Locate every blood parasite and identify its species.
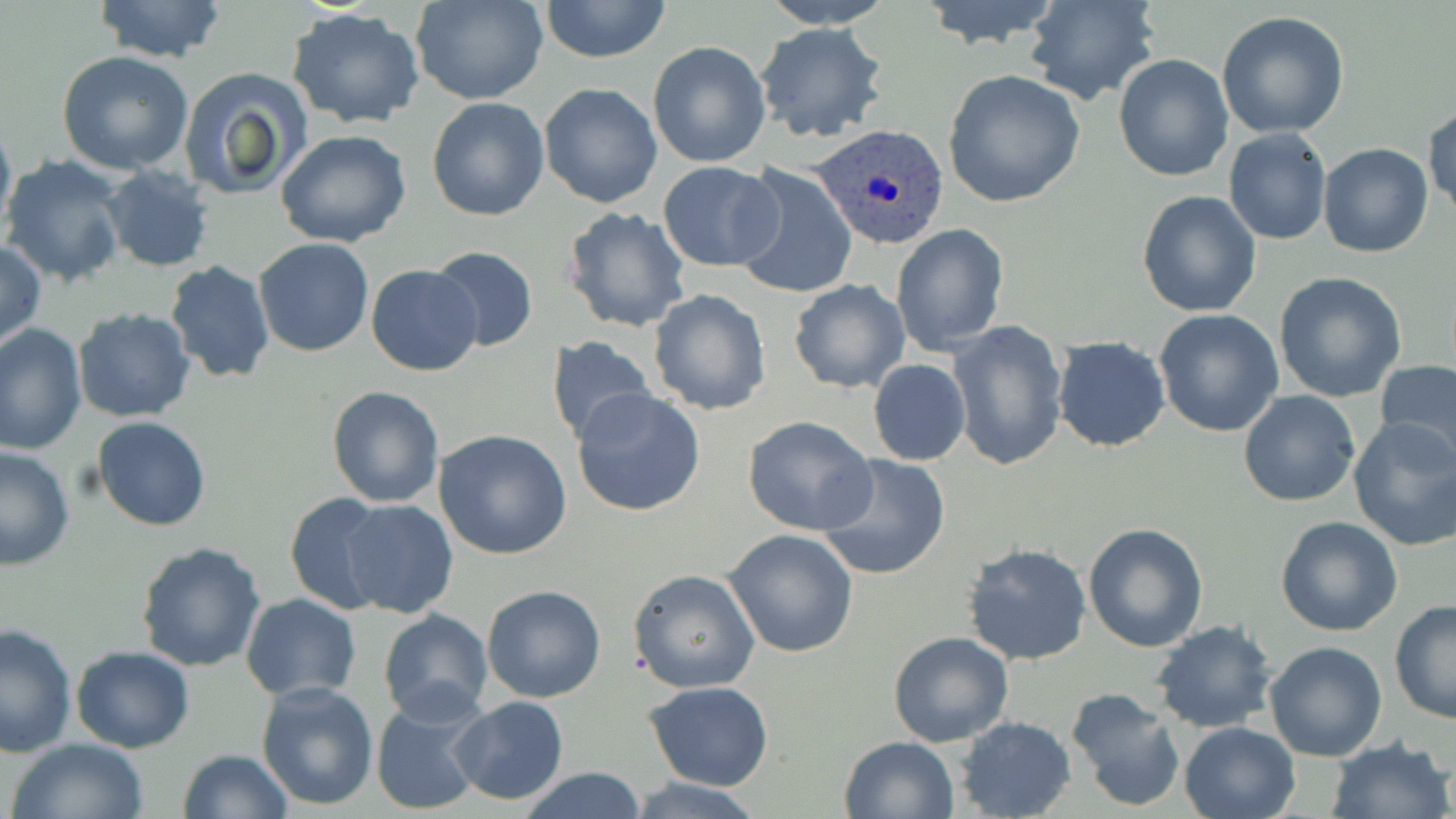

Approximate bounding boxes as (x1,y1)-(x2,y2) corner pairs in pixels.
Plasmodium ovale-infected red blood cells: (812,125)-(952,250).
No Plasmodium falciparum, Plasmodium malariae, Plasmodium vivax, Babesia divergens, or Trypanosoma brucei observed.

{
  "slide_level_diagnosis": "Plasmodium ovale",
  "field_of_view": "single",
  "modality": "optical microscopy",
  "magnification": "1000x",
  "stain": "May-Grünwald-Giemsa",
  "preparation": "thin blood smear",
  "uninfected_red_blood_cell_locations": "approximate bounding boxes as (x1,y1)-(x2,y2) corner pairs in pixels: (93,0)-(229,63), (413,0)-(550,105), (539,0)-(671,63), (758,0)-(899,28), (917,0)-(1066,52), (1023,0)-(1162,105), (285,8)-(427,129), (1217,11)-(1349,138), (756,22)-(888,143), (647,40)-(772,169), (57,50)-(195,175), (1113,54)-(1233,182), (178,67)-(310,200), (942,69)-(1086,209), (539,82)-(664,209), (426,96)-(549,221), (1424,104)-(1456,219), (0,112)-(16,240), (1224,128)-(1331,245), (275,129)-(412,248), (1318,142)-(1435,258), (2,155)-(130,288), (658,160)-(782,272), (731,163)-(857,300), (101,167)-(216,271), (1136,189)-(1263,319), (561,206)-(691,334), (891,222)-(1009,356), (1,238)-(46,350), (254,238)-(374,356), (429,246)-(539,350), (164,260)-(275,383), (366,265)-(484,377), (1272,271)-(1407,403), (788,279)-(910,394), (648,289)-(771,415), (72,306)-(195,423), (1153,309)-(1284,437), (949,321)-(1071,472), (0,324)-(87,458), (546,335)-(658,447), (1052,336)-(1171,452), (867,359)-(971,467), (1375,362)-(1456,466), (326,385)-(444,507), (571,387)-(707,517), (1239,390)-(1361,508), (742,415)-(877,535), (93,416)-(211,531), (1347,416)-(1456,551), (433,429)-(573,560), (0,445)-(77,571), (818,453)-(951,581), (284,491)-(389,616), (339,500)-(459,618), (1275,516)-(1404,637), (1082,521)-(1210,652), (723,527)-(859,659), (137,540)-(268,671), (965,542)-(1092,666), (629,569)-(760,694), (481,584)-(606,703), (240,594)-(362,700), (1388,600)-(1455,723), (377,607)-(494,722), (1151,620)-(1278,734), (0,621)-(77,758), (888,630)-(1014,748), (1264,640)-(1387,761), (70,645)-(193,752), (256,680)-(381,811), (645,680)-(773,790), (1065,687)-(1187,812), (369,692)-(490,816), (449,698)-(569,804), (954,717)-(1075,819), (1179,721)-(1301,819), (839,736)-(959,819), (1327,736)-(1452,819), (7,738)-(150,819), (177,749)-(292,819), (520,767)-(648,819), (626,775)-(771,819)",
  "image_size": "1456×819 pixels"
}